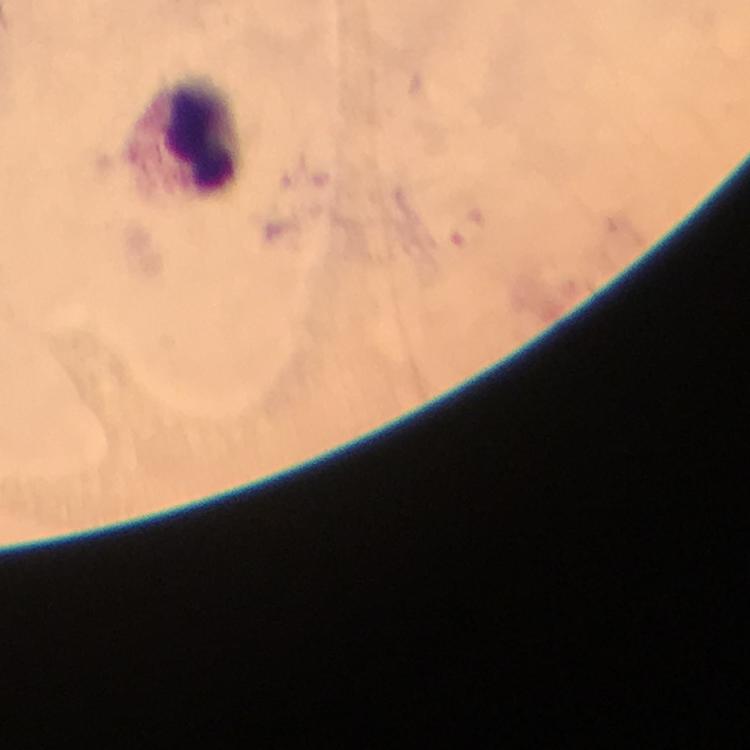

{
  "preparation": "thick blood film",
  "immersion_oil": "applied",
  "stain": "Giemsa",
  "cropped_from": "a single field of view",
  "context": "from a malaria diagnostic workup",
  "magnification": "100x",
  "plasmodium_parasites": "none seen",
  "capture": "smartphone camera through the microscope",
  "image_size": "750×750 pixels",
  "leukocyte_locations": "approximate centers as (x, y) in pixels: (183, 133)"
}